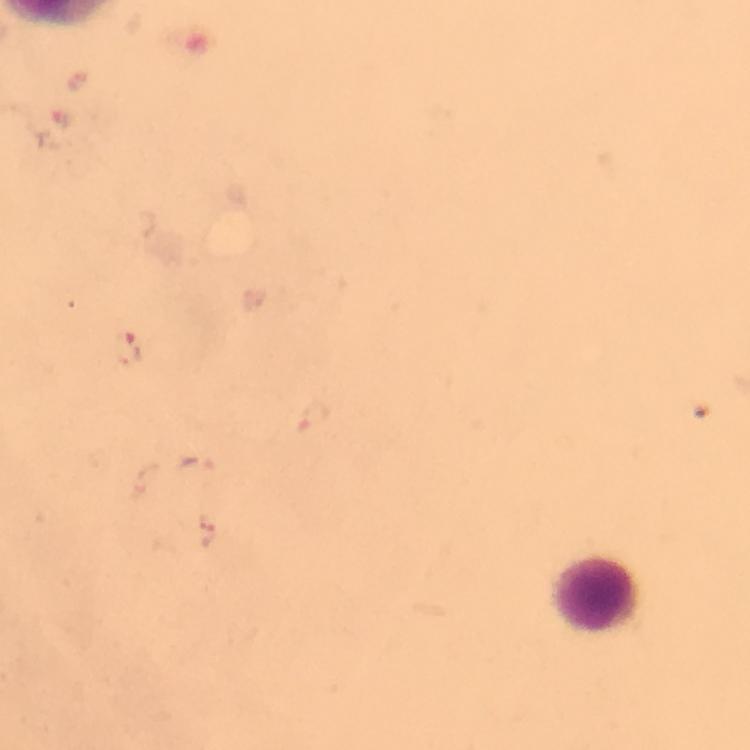
image size = 750×750 pixels
magnification = 100x
capture = smartphone mounted on the microscope
context = from a diagnostic examination for malaria
cropped from = a single field of view
leukocyte locations = approximate object centers, in pixels from the top-left corner: (x=600, y=596)
immersion oil = used
Plasmodium parasite locations = approximate object centers, in pixels from the top-left corner: (x=62, y=117), (x=132, y=350), (x=317, y=418), (x=196, y=464), (x=206, y=530)
preparation = thick blood film
stain = Giemsa